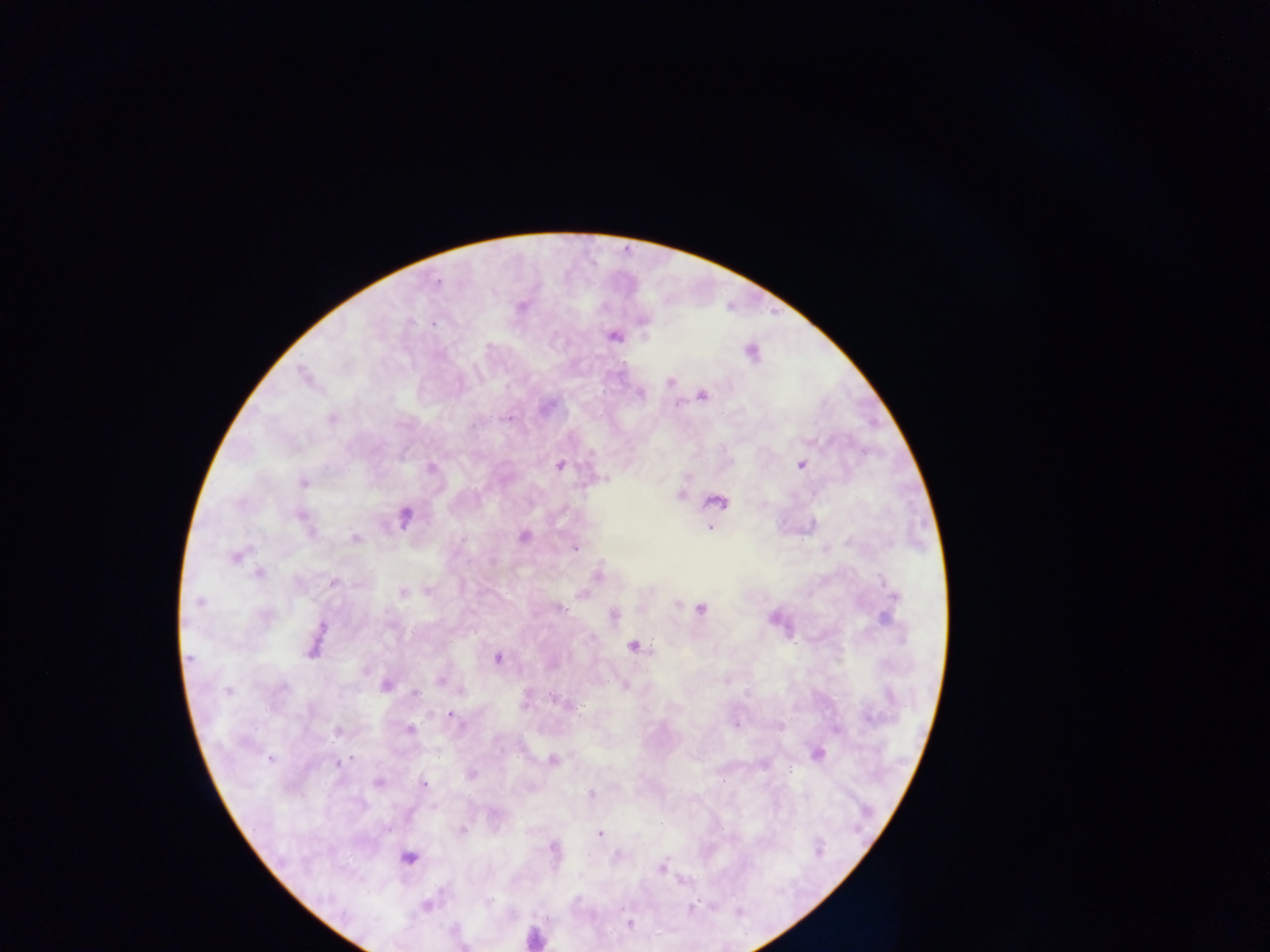
preparation = thick blood film
field of view = single
image size = 1270×952 pixels
Plasmodium parasite locations = approximate centers as (x, y) in pixels: (437, 282), (520, 307), (642, 320), (613, 335), (751, 352), (304, 376), (670, 382), (639, 392), (702, 394), (331, 417), (508, 418), (800, 463), (560, 464), (431, 467), (302, 482), (678, 495), (716, 501), (403, 516), (300, 517), (709, 528), (523, 536), (355, 539), (573, 547), (235, 556), (258, 573), (597, 575), (333, 582), (401, 592), (894, 597), (199, 602), (700, 608), (613, 614), (316, 641), (632, 645), (497, 658), (441, 680), (385, 685), (624, 685), (227, 690), (415, 694), (563, 704), (450, 715), (409, 729), (337, 731), (817, 754), (271, 759), (552, 761), (340, 762), (471, 774), (378, 782), (424, 784), (461, 831), (599, 834), (409, 858), (661, 867), (427, 905), (629, 924)
capture = mobile-phone photograph through a microscope
leukocyte locations = approximate centers as (x, y) in pixels: (534, 937)
country = Ghana